Assess the morphology of the red blood cells.
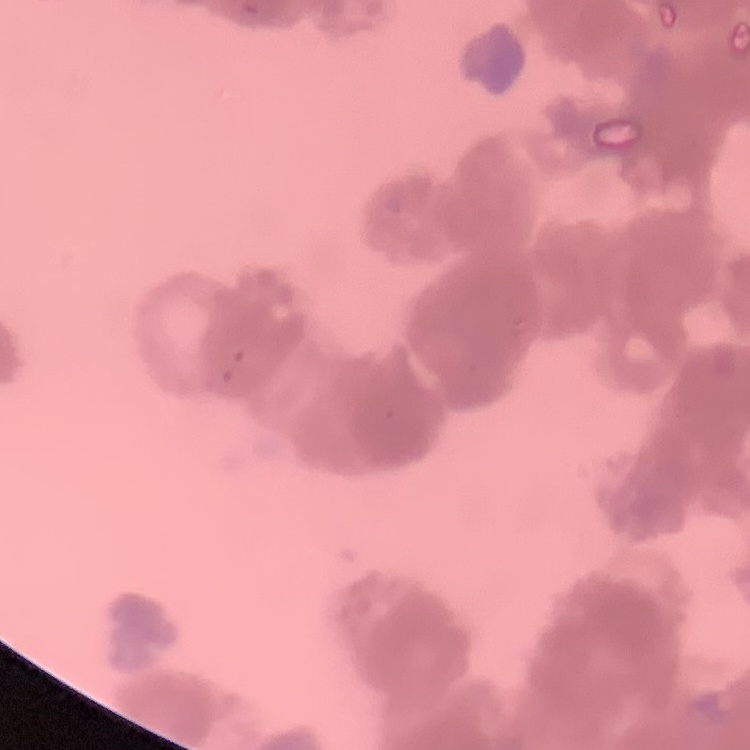

They show rouleaux formation.

stain = Field's or Giemsa
preparation = thin peripheral smear
image type = one tile cut from a larger photomicrograph